Classify this cell by malaria status.
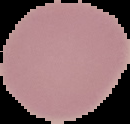

Uninfected.

From a thin blood smear. Image is 130×124 pixels. The area outside the segmented cell region is set to black.